Name the parasite shown.
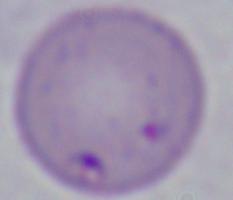

Babesia.

Summary:
  - Modality: photomicrograph
  - Magnification: 1000x